Report the malaria status of this cell.
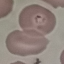

It is parasitized.

Summary:
  - Image type: automatically extracted cell patch, resized to 64 × 64 pixels
  - Preparation: thin smear
  - Stain: Giemsa
  - Capture: smartphone camera at the microscope eyepiece